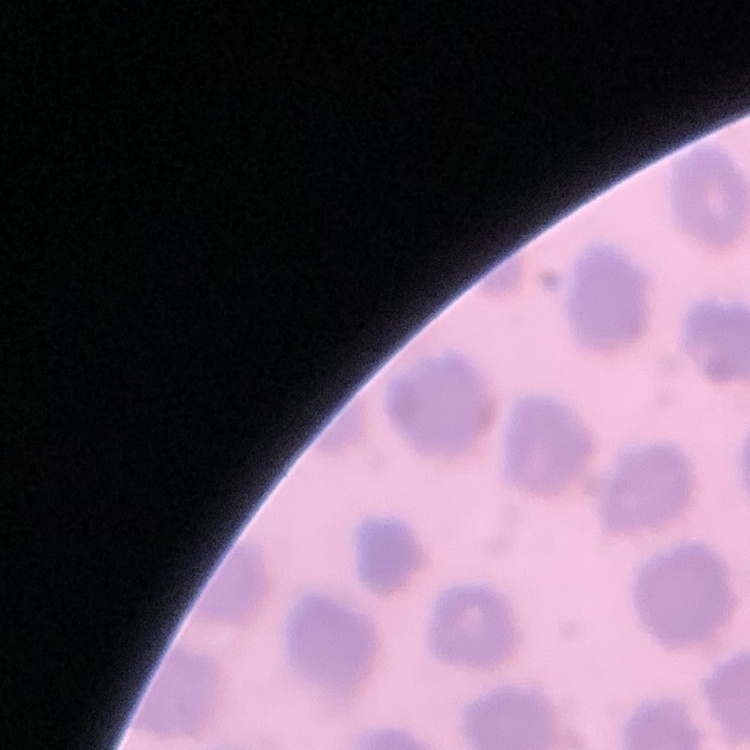
Summary:
  - Erythrocyte morphology: no rouleaux formation
  - Preparation: thin blood film
  - Stain: Field's or Giemsa
  - Image type: one tile cut from a larger photomicrograph